Point out each Plasmodium parasite and each leukocyte.
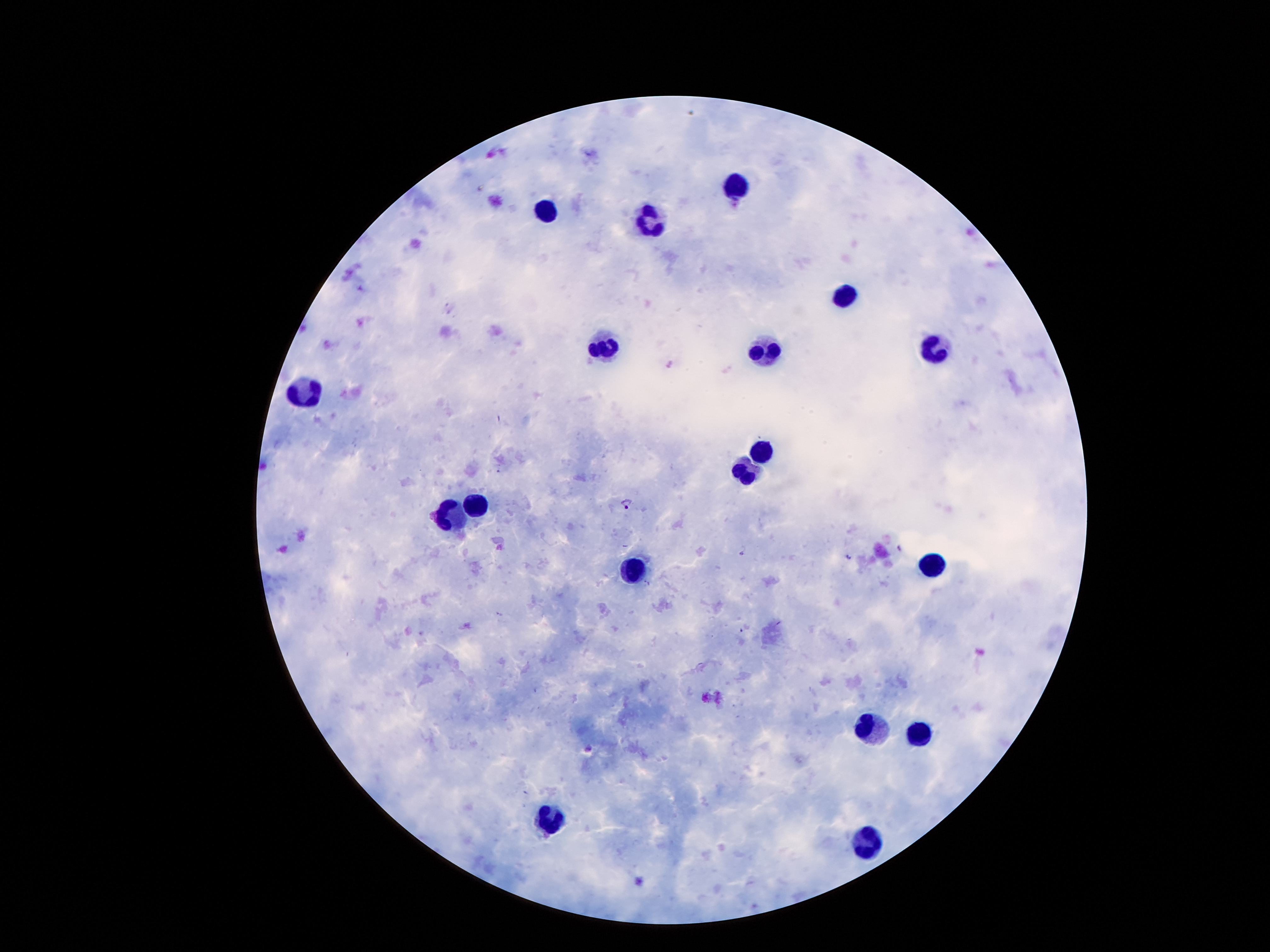

Approximate centers as (x, y) in pixels.
Plasmodium parasites: (627, 503), (849, 557).
Leukocytes: (739, 186), (543, 203), (651, 223), (846, 292), (768, 347), (602, 350), (938, 350), (307, 391), (756, 449), (746, 470), (473, 504), (451, 517), (936, 566), (631, 568), (875, 726), (922, 732), (549, 822), (868, 838).

Photographed through the microscope eyepiece with a smartphone camera. Patient malaria status: infected with Plasmodium falciparum. One field from this slide. Image is 1270×952 pixels. Thick blood smear. Giemsa stain. 100x magnification.